Classify this cell by malaria status.
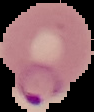

It is parasitized.

{
  "preparation": "thin blood smear",
  "image_size": "94×112 pixels",
  "image_type": "cell region segmented out of the field of view; surrounding area masked to black"
}